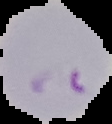

From a thin blood smear. Malaria status: parasitized. Image is 112×124 pixels. The area outside the segmented cell region is set to black.